Assess this cell for malaria.
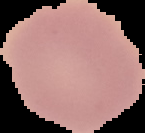

It is uninfected.

preparation = thin blood film
image size = 145×133 pixels
image type = cell region segmented out of the field of view; surrounding area masked to black